State which parasite is depicted.
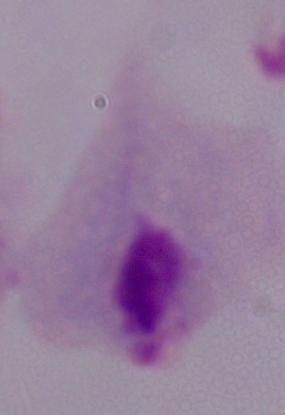
This is a trichomonad.

magnification = 1000x
modality = micrograph